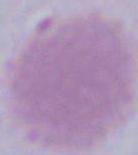

Summary:
  - Identification: erythrocyte
  - Magnification: 1000x
  - Modality: photomicrograph